Assess the morphology of the erythrocytes.
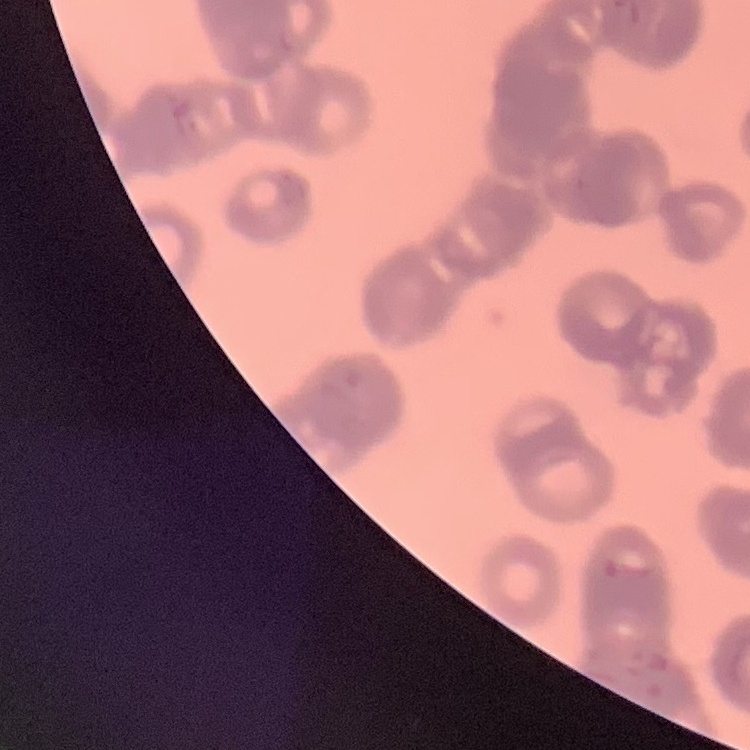
They show rouleaux formation.

preparation: thin blood smear
image_type: one tile cut from a larger photomicrograph
stain: Field's or Giemsa